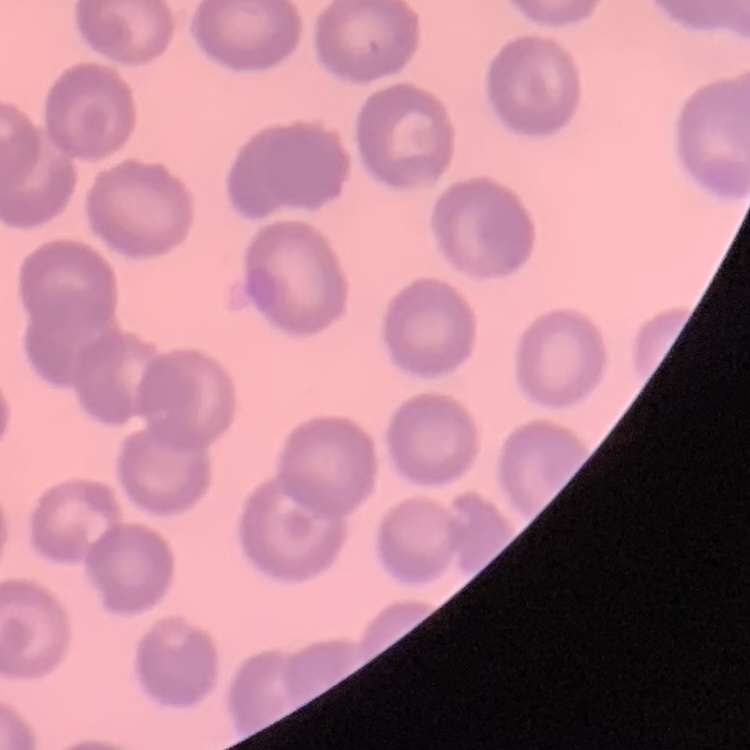

Summary:
  - Erythrocyte morphology: no rouleaux formation
  - Image type: square crop of a larger photomicrograph
  - Stain: Field's or Giemsa
  - Preparation: thin blood film